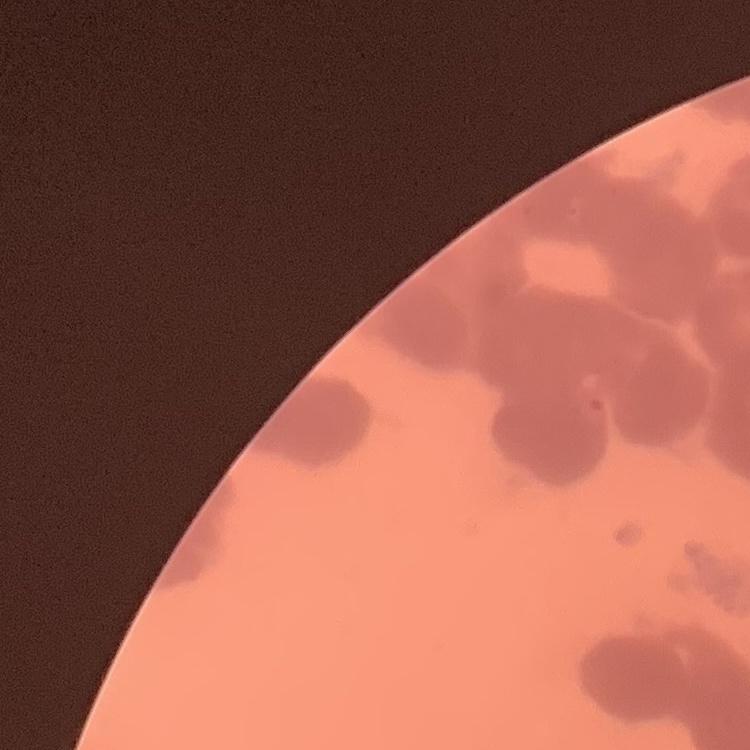
The red blood cells show rouleaux formation. Field's or Giemsa stain. Thin blood film. One tile cut from a larger photomicrograph.